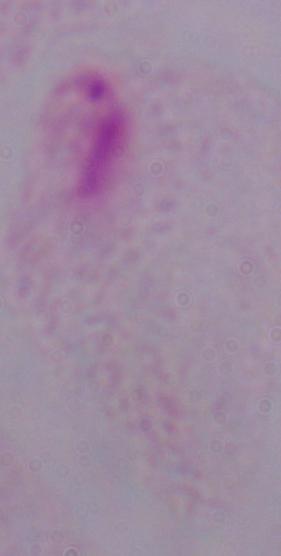
modality = micrograph
magnification = 1000x
identification = trichomonad